Classify this cell by malaria status.
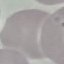

It is uninfected.

stain: Giemsa
image_type: cell patch, automatically extracted from a larger field of view and resized to 64 × 64 pixels
capture: smartphone through the microscope eyepiece
preparation: thin blood smear